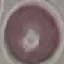

Summary:
  - Malaria status: uninfected
  - Stain: Giemsa
  - Image type: cell patch, automatically extracted from a larger field of view and resized to 64 × 64 pixels
  - Preparation: thin blood film
  - Capture: smartphone camera at the microscope eyepiece